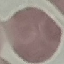
Summary:
  - Malaria status: uninfected
  - Capture: smartphone camera at the microscope eyepiece
  - Preparation: thin blood smear
  - Stain: Giemsa
  - Image type: cell patch, automatically extracted from a larger field of view and resized to 64 × 64 pixels